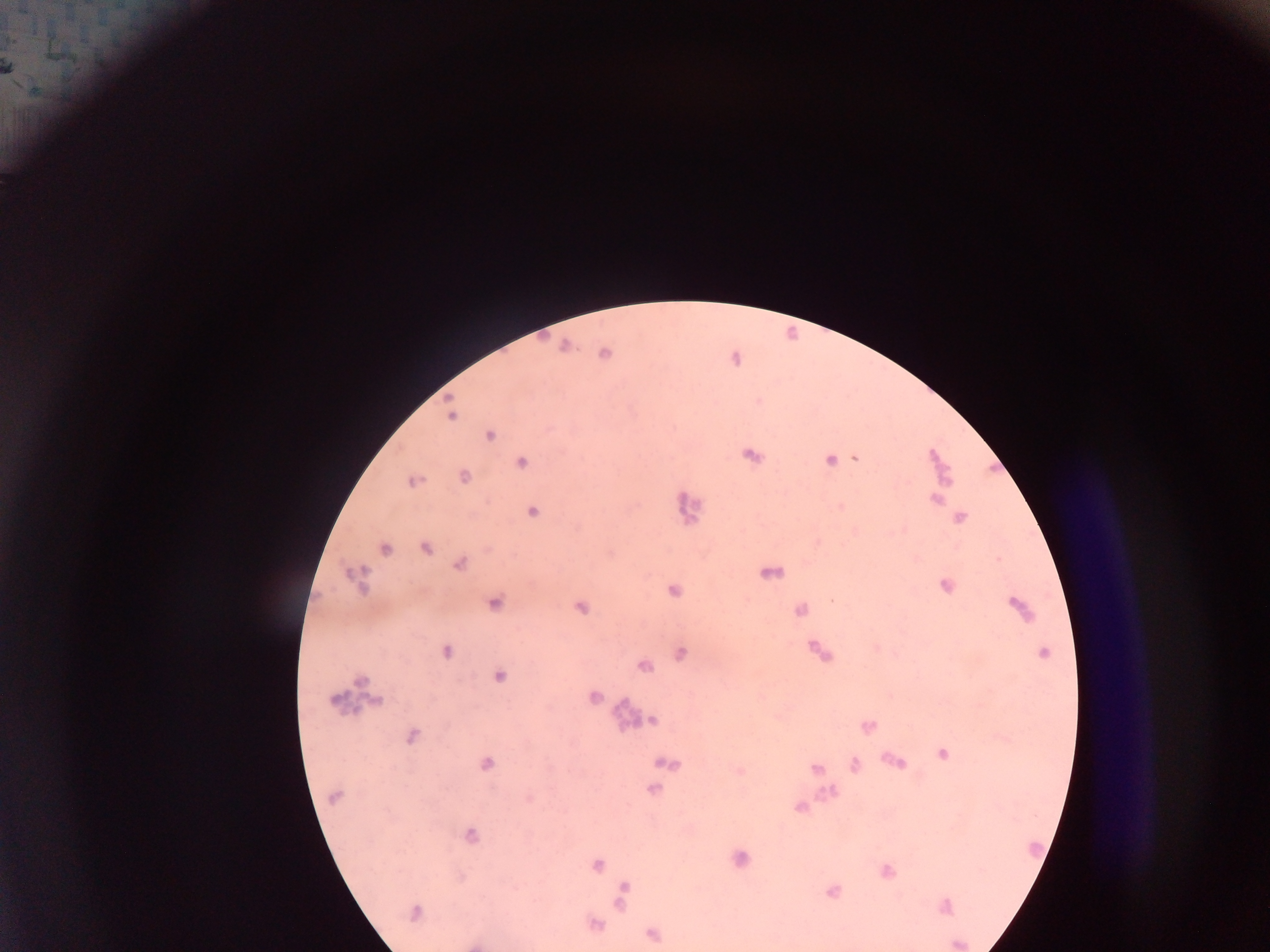 Approximate centers as x y in pixels. Plasmodium parasite locations: 10 68; 464 476; 413 481; 831 599; 411 736; 486 765; 334 798; 529 799; 472 835. Thick blood film. Image is 1270×952 pixels. One field of view. Collected in Ghana. Mobile-phone photograph taken through the microscope.